Name the parasite shown.
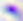

This is Toxoplasma gondii.

magnification = 400x
modality = photomicrograph